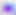

400x magnification. Toxoplasma gondii is shown. Photomicrograph.